Point out each leukocyte.
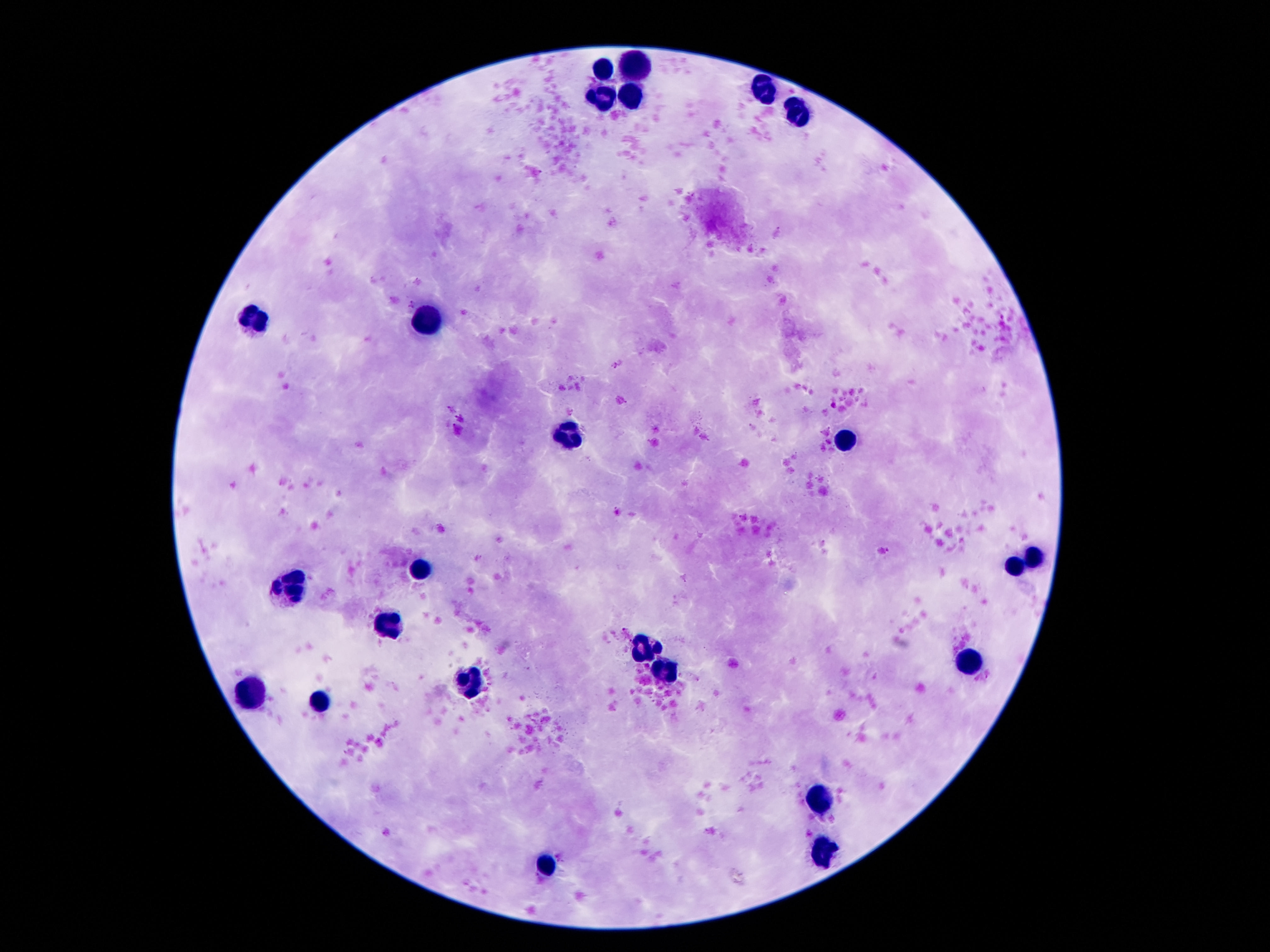
Approximate centers as {x, y} in pixels.
Leukocytes: {635, 66}, {604, 72}, {764, 90}, {628, 94}, {601, 98}, {798, 112}, {428, 319}, {255, 322}, {562, 437}, {846, 440}, {1035, 558}, {1014, 566}, {418, 573}, {291, 586}, {389, 624}, {643, 649}, {969, 660}, {662, 668}, {473, 687}, {257, 697}, {323, 702}, {822, 797}, {825, 851}, {546, 870}.

Summary:
  - Capture: smartphone camera through the microscope eyepiece
  - Image size: 1270×952 pixels
  - Field of view: single
  - Patient malaria status: not infected
  - Magnification: 100x
  - Preparation: thick blood smear
  - Stain: Giemsa